Assess the morphology of the erythrocytes.
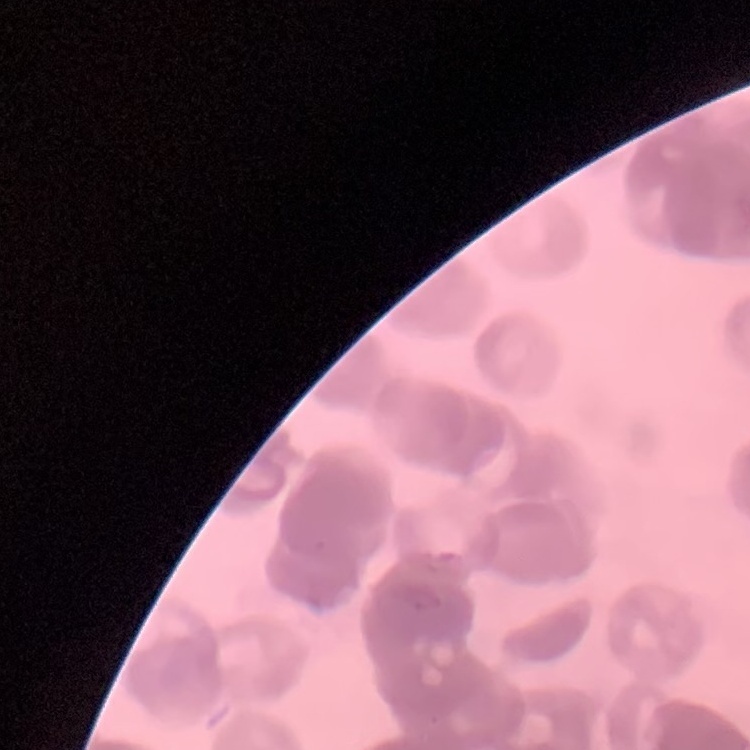

They show rouleaux formation.

Summary:
  - Image type: square crop of a larger photomicrograph
  - Preparation: thin blood smear
  - Stain: Field's or Giemsa